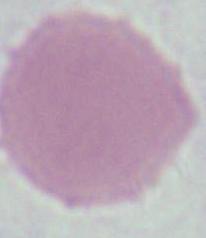
{
  "identification": "red blood cell",
  "modality": "micrograph",
  "magnification": "1000x"
}